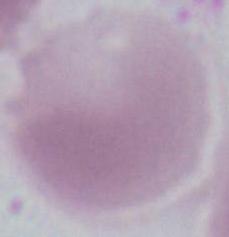

Summary:
  - Modality: micrograph
  - Magnification: 1000x
  - Identification: erythrocyte